Report the malaria status of this cell.
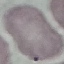
Uninfected.

Summary:
  - Stain: Giemsa
  - Image type: automatically extracted cell patch, resized to 64 × 64 pixels
  - Capture: smartphone through the microscope eyepiece
  - Preparation: thin blood smear